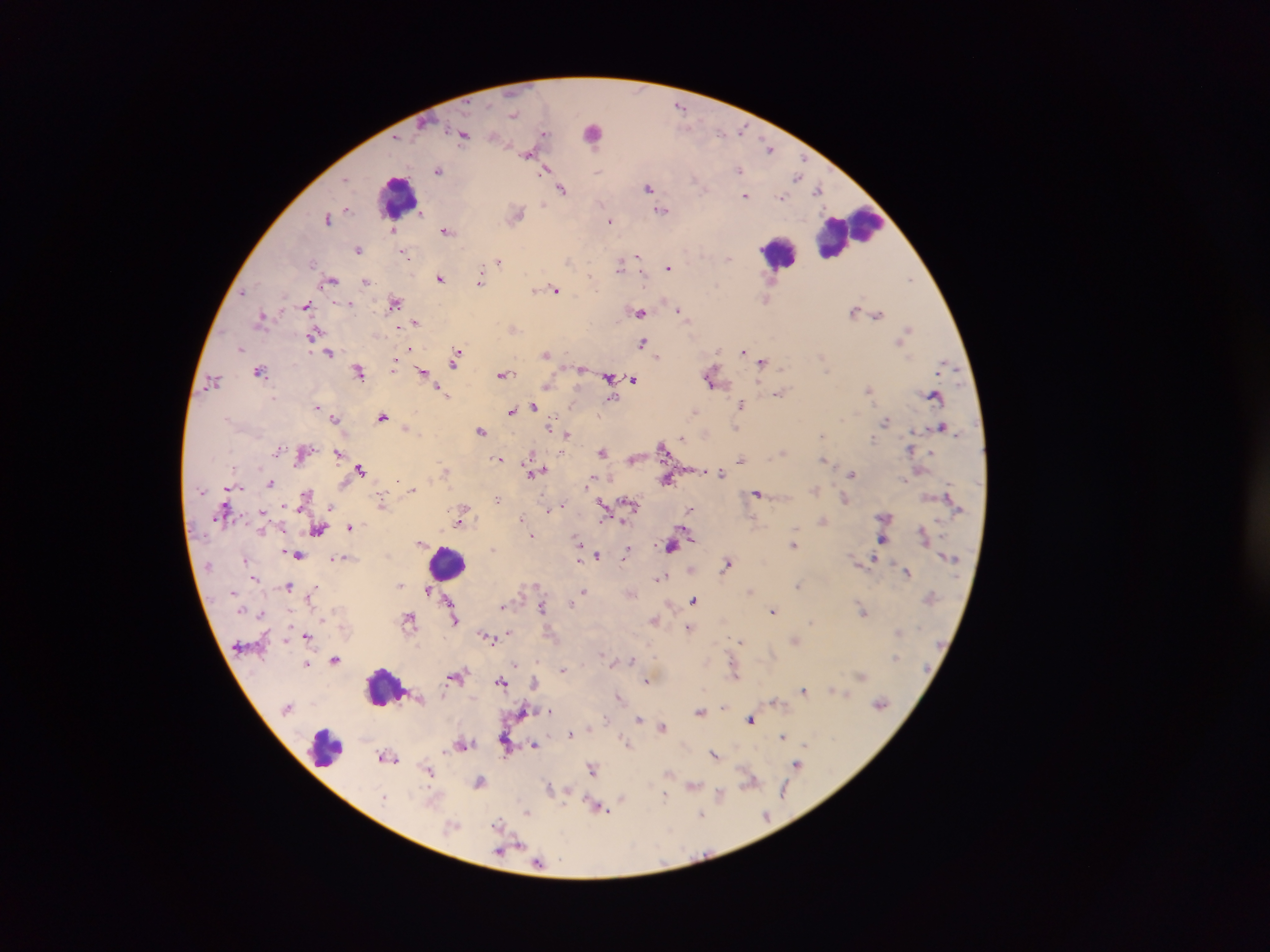

Approximate centers as (x, y) in pixels. Malaria parasite locations: (681, 106), (514, 113), (545, 132), (464, 133), (770, 148), (529, 152), (740, 169), (439, 170), (546, 170), (599, 170), (798, 176), (558, 183), (649, 187), (562, 188), (819, 189), (745, 195), (782, 197), (662, 209), (346, 210), (517, 213), (329, 217), (610, 220), (392, 230), (446, 230), (359, 249), (403, 251), (639, 257), (729, 258), (498, 261), (621, 265), (669, 267), (441, 277), (481, 279), (331, 280), (909, 280), (366, 281), (555, 290), (244, 291), (767, 298), (394, 302), (349, 303), (307, 304), (639, 311), (855, 311), (681, 312), (877, 313), (262, 317), (416, 322), (513, 328), (907, 331), (314, 333), (902, 339), (643, 343), (241, 348), (410, 348), (744, 351), (546, 352), (330, 353), (658, 355), (756, 356), (457, 357), (762, 361), (944, 364), (394, 365), (581, 367), (360, 370), (260, 371), (423, 373), (504, 374), (712, 376), (609, 378), (633, 378), (212, 381), (547, 384), (442, 390), (869, 391), (779, 393), (935, 395), (613, 398), (742, 404), (317, 406), (534, 407), (513, 410), (694, 411), (383, 416), (335, 417), (886, 421), (406, 426), (550, 426), (942, 426), (481, 429), (567, 434), (822, 435), (874, 439), (664, 446), (911, 448), (279, 450), (603, 451), (783, 452), (339, 453), (532, 455), (500, 458), (634, 459), (824, 459), (741, 460), (360, 469), (701, 470), (446, 471), (537, 471), (722, 472), (853, 474), (592, 479), (668, 479), (271, 482), (413, 489), (306, 495), (758, 495), (498, 498), (844, 498), (382, 502), (629, 503), (604, 504), (283, 505), (560, 506), (465, 508), (690, 509), (549, 510), (265, 511), (884, 517), (521, 518), (461, 519), (823, 520), (350, 526), (319, 529), (924, 534), (533, 535), (884, 538), (580, 541), (422, 543), (794, 544), (671, 545), (298, 553), (598, 554), (627, 555), (345, 557), (580, 557), (335, 558), (874, 558), (728, 564), (907, 572), (255, 577), (660, 577), (400, 584), (799, 584), (290, 585), (535, 585), (429, 589), (750, 590), (584, 591), (632, 593), (310, 598), (695, 599), (572, 604), (504, 605), (543, 607), (863, 610), (774, 611), (322, 619), (410, 619), (456, 619), (655, 619), (813, 622), (688, 627), (510, 631), (899, 632), (307, 636), (490, 637), (795, 639), (741, 640), (336, 659), (631, 659), (614, 661), (518, 663), (307, 664), (563, 669), (735, 673), (456, 675), (861, 675), (646, 680), (502, 682), (535, 683), (803, 691), (839, 691), (846, 693), (442, 695), (618, 695), (775, 702), (881, 703), (551, 710), (700, 711), (640, 717), (751, 719), (590, 726), (662, 726), (570, 733), (783, 734), (628, 743), (463, 744), (506, 744), (535, 744), (716, 754), (387, 757), (798, 764), (592, 768), (430, 770), (670, 772), (751, 780), (480, 782), (693, 785), (550, 789), (784, 789), (567, 791), (720, 793), (665, 795), (622, 797), (599, 807), (528, 812), (702, 814), (766, 814), (498, 825), (519, 844), (512, 847), (539, 864). Leukocyte locations: (593, 131), (399, 196), (849, 232), (779, 252), (449, 564), (387, 687), (324, 748). Sample from Ghana. Thick blood smear. Mobile-phone photograph taken through the microscope. Image is 1270×952 pixels. Single field of view.